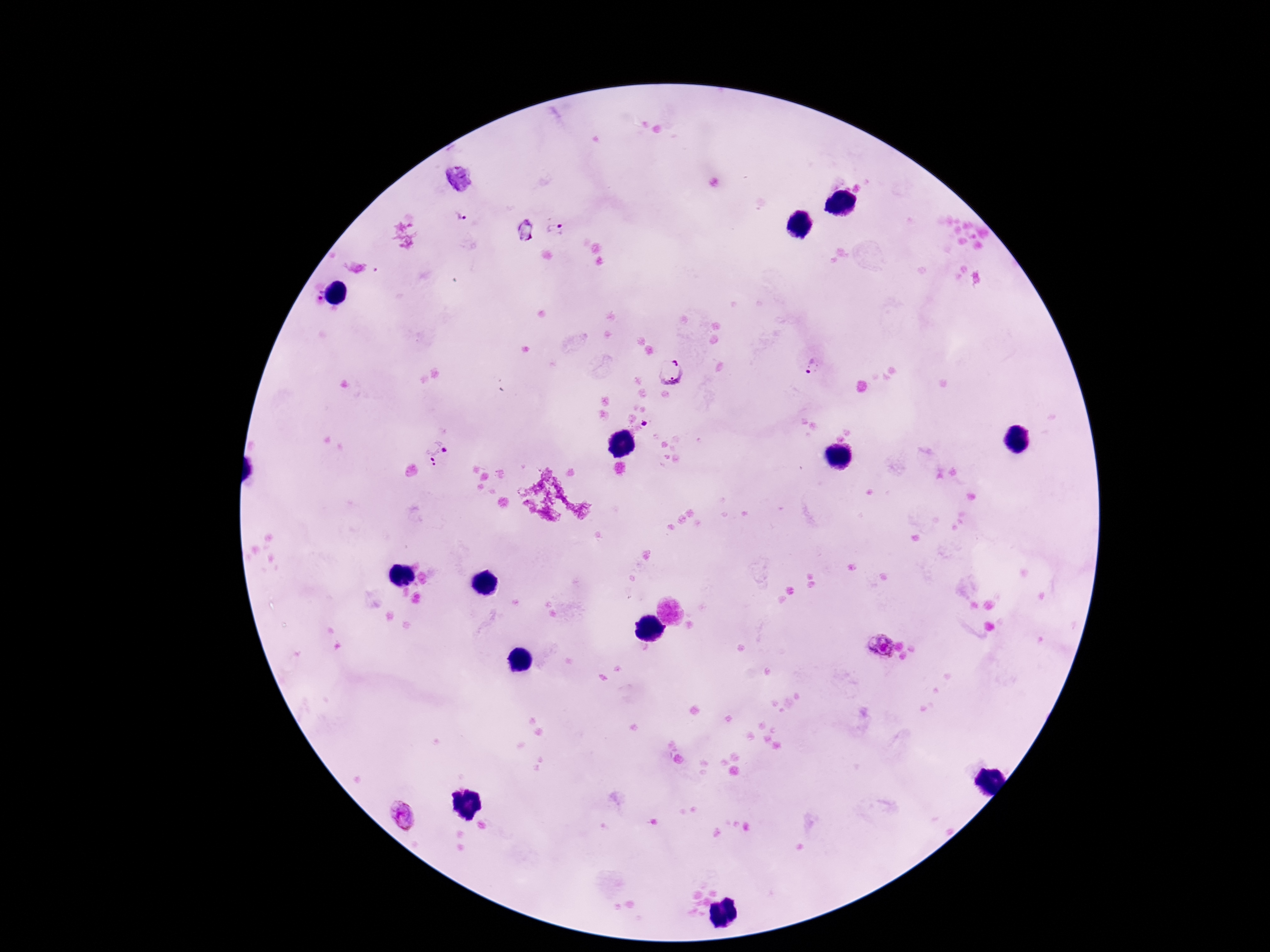

Approximate centers as {x, y} in pixels.
Summary:
  - Plasmodium parasite locations: {459, 216}, {555, 230}, {319, 294}, {814, 367}, {670, 371}, {436, 453}, {881, 644}, {404, 813}
  - Capture: smartphone camera through the microscope eyepiece
  - Field of view: one from this slide
  - Magnification: 100x
  - Patient malaria status: positive
  - Preparation: thick blood film
  - Stain: Giemsa
  - Image size: 1270×952 pixels